Identify the parasite.
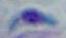

This is Toxoplasma gondii.

Summary:
  - Magnification: 1000x
  - Modality: micrograph